Classify this cell by malaria status.
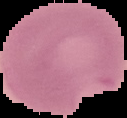

Parasitized.

image size = 127×118 pixels
image type = segmented cell region on a black background
preparation = thin blood film